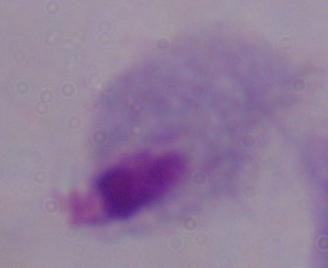
magnification = 1000x
identification = trichomonad
modality = photomicrograph